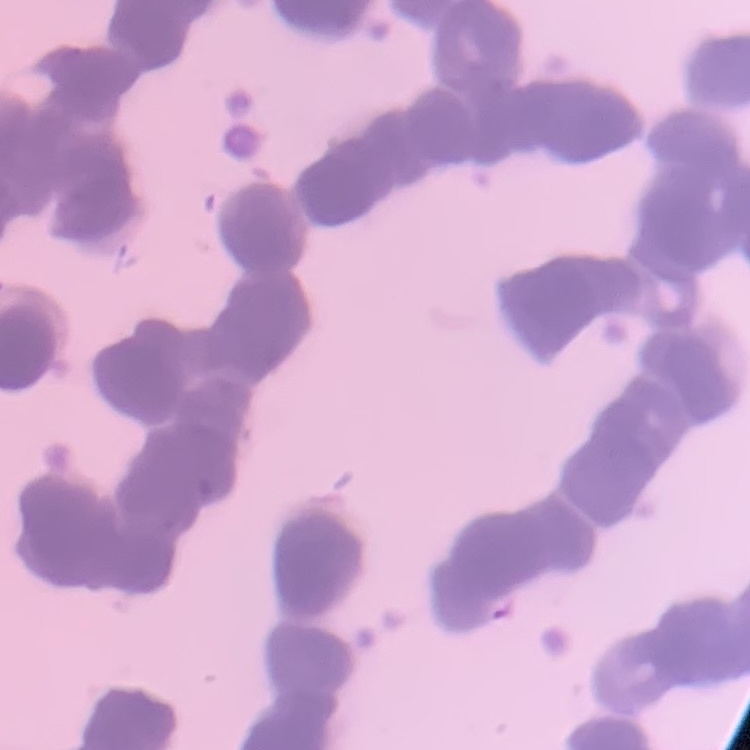
Summary:
  - Red blood cell morphology: rouleaux formation
  - Stain: Field's or Giemsa
  - Image type: one tile cut from a larger photomicrograph
  - Preparation: thin blood smear